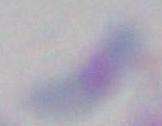

Summary:
  - Magnification: 1000x
  - Identification: Toxoplasma gondii
  - Modality: micrograph